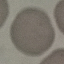
Summary:
  - Malaria status: uninfected
  - Image type: cell patch, automatically extracted from a larger field of view and resized to 64 × 64 pixels
  - Capture: smartphone through the microscope eyepiece
  - Stain: Giemsa
  - Preparation: thin blood film